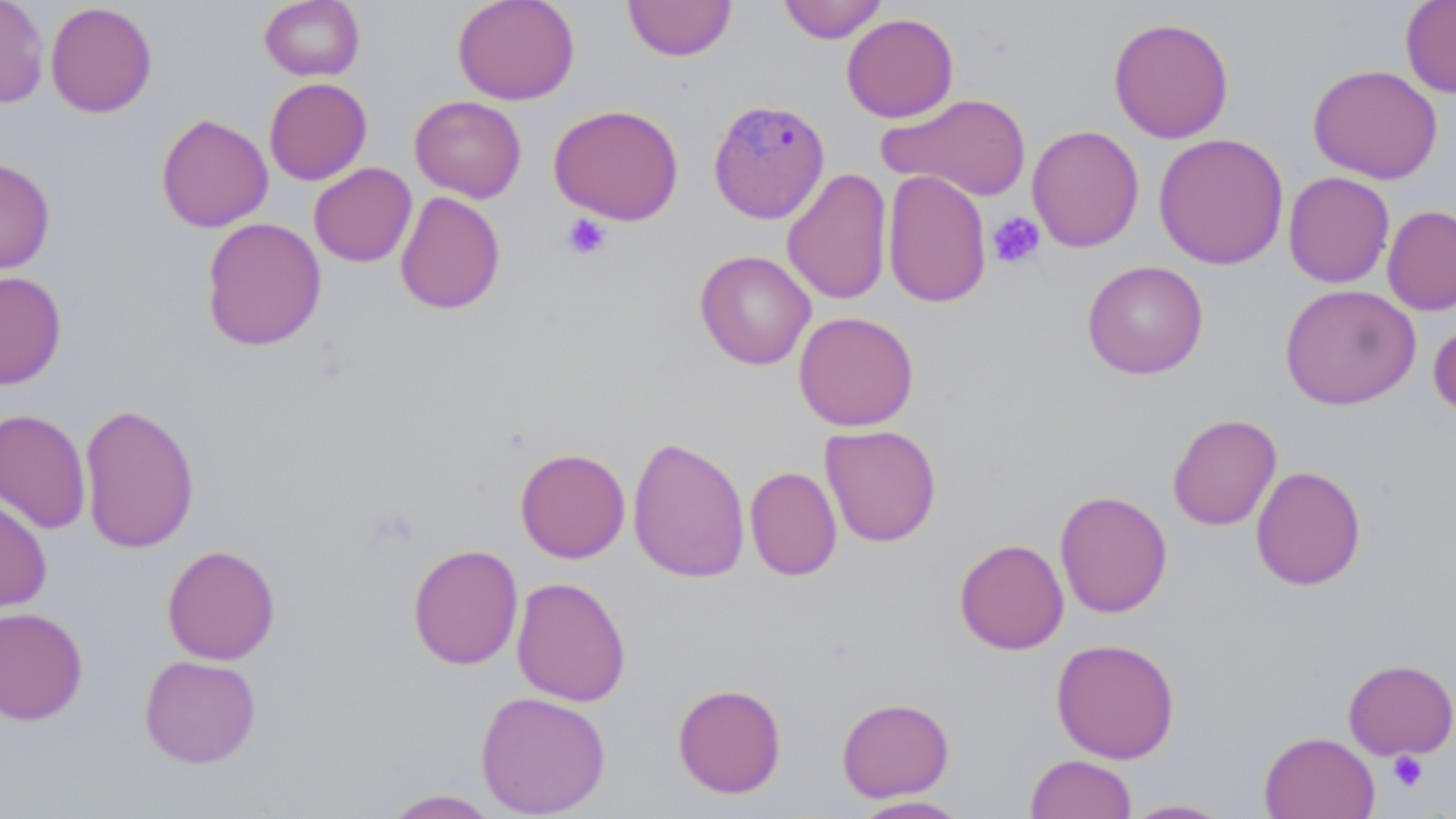
slide-level diagnosis = Plasmodium malariae
magnification = 1000x
stain = May-Grünwald-Giemsa
field of view = single
modality = optical microscopy
uninfected red blood cell locations = approximate bounding boxes as (x1,y1)-(x2,y2) corner pairs in pixels: (0,0)-(49,107), (259,0)-(365,81), (452,0)-(580,105), (623,0)-(737,61), (777,0)-(888,44), (1400,0)-(1456,98), (45,2)-(157,117), (841,13)-(959,123), (1108,16)-(1235,143), (1307,64)-(1443,185), (264,77)-(372,185), (879,93)-(1033,201), (410,95)-(527,202), (548,104)-(684,225), (155,113)-(273,232), (1027,125)-(1144,252), (1153,132)-(1289,270), (0,157)-(55,274), (308,162)-(416,267), (782,168)-(893,305), (882,169)-(992,308), (1283,171)-(1395,288), (394,191)-(505,315), (1382,204)-(1456,316), (201,216)-(326,351), (694,250)-(816,370), (1082,260)-(1209,380), (0,271)-(67,389), (1280,283)-(1420,410), (793,311)-(919,431), (1429,318)-(1456,420), (79,402)-(200,554), (0,408)-(91,534), (1167,413)-(1282,531), (820,424)-(942,547), (627,435)-(751,583), (515,447)-(630,563), (1250,465)-(1367,590), (745,466)-(842,581), (1055,489)-(1173,619), (0,493)-(52,613), (954,538)-(1069,654), (408,543)-(523,670), (161,544)-(280,665), (512,576)-(631,707), (0,605)-(88,725), (1051,638)-(1180,763), (139,654)-(261,768), (1342,658)-(1456,760), (672,683)-(786,798), (475,690)-(611,818), (836,696)-(955,801), (1259,731)-(1380,819), (1025,753)-(1137,818), (380,788)-(501,818), (851,795)-(973,818), (1122,798)-(1235,818)
platelet locations = approximate bounding boxes as (x1,y1)-(x2,y2) corner pairs in pixels: (987,211)-(1046,269), (561,213)-(612,261), (1387,751)-(1427,791)
image size = 1456×819 pixels
preparation = thin blood film
Plasmodium malariae-infected red blood cell locations = approximate bounding boxes as (x1,y1)-(x2,y2) corner pairs in pixels: (707,98)-(830,224)